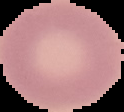

Image is 124×112 pixels. From a thin blood smear. Malaria status: uninfected. Segmented cell region on a black background.